Assess the morphology of the erythrocytes.
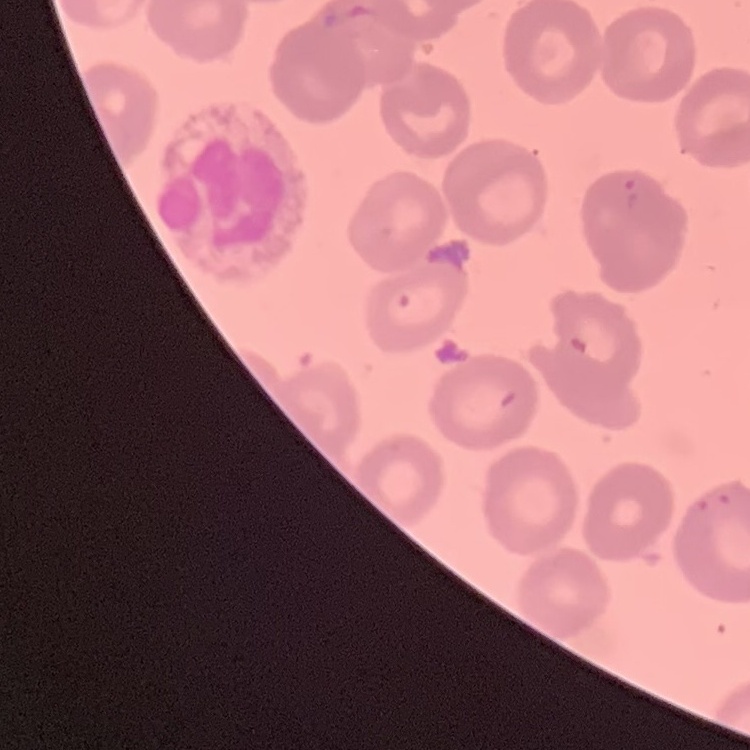

No rouleaux formation.

Square crop of a larger photomicrograph. Thin peripheral smear. Field's or Giemsa stain.